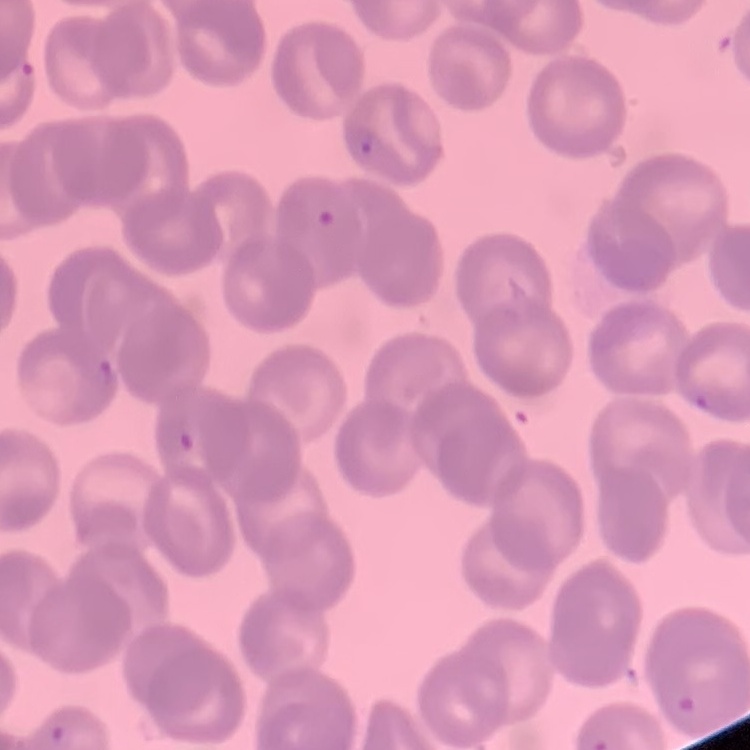
red blood cell morphology = rouleaux formation
preparation = thin peripheral smear
stain = Field's or Giemsa
image type = square crop of a larger photomicrograph